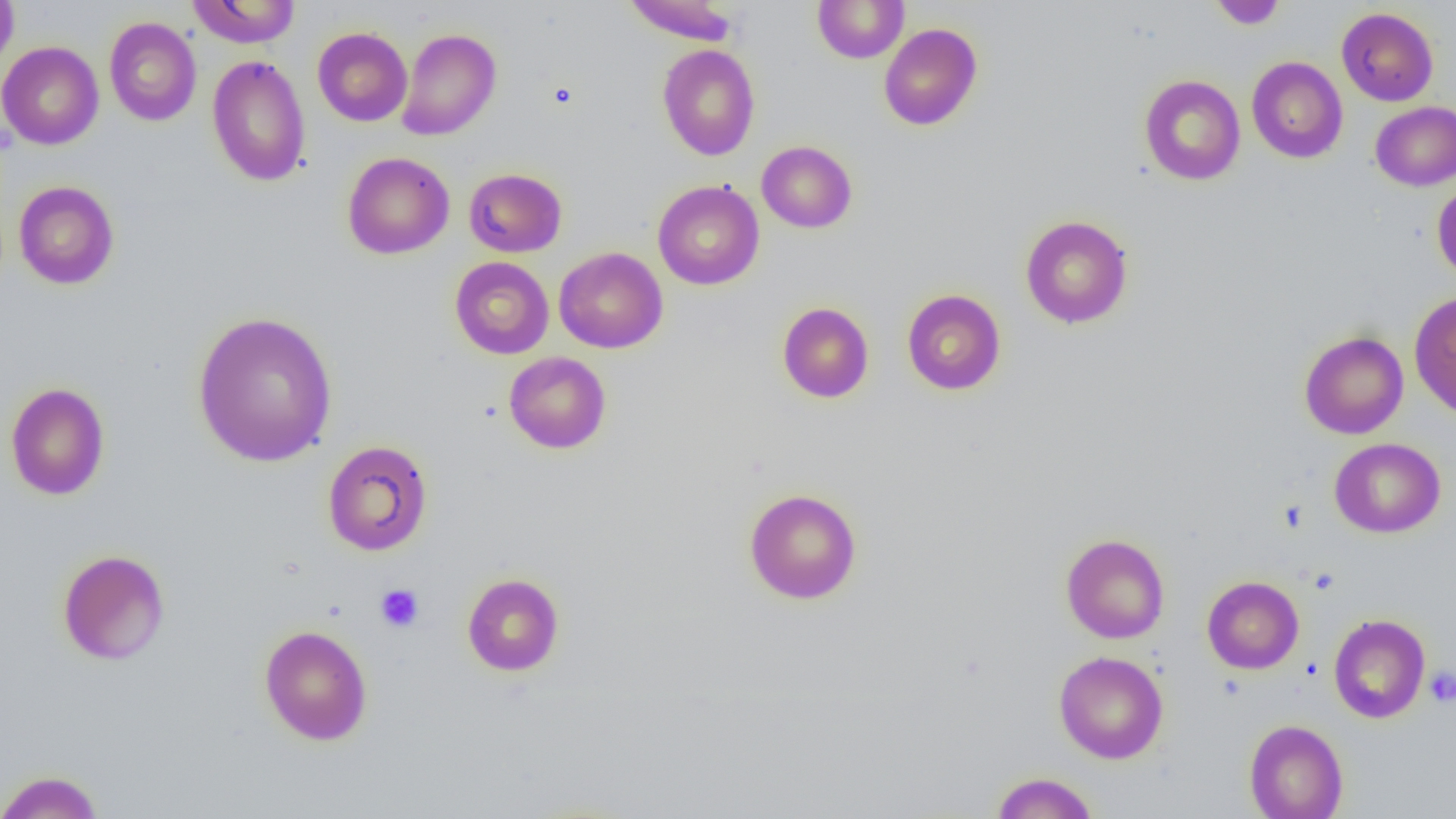
Approximate bounding boxes as [x1, y1, x2, y2] in pixels. Platelet locations: [548, 81, 578, 109], [375, 584, 424, 632], [1425, 666, 1456, 706]. Uninfected red blood cell locations: [0, 0, 19, 78], [187, 0, 300, 48], [622, 0, 739, 45], [812, 0, 909, 63], [1208, 1, 1287, 30], [1337, 7, 1438, 106], [104, 17, 202, 126], [878, 23, 982, 131], [313, 27, 412, 127], [396, 28, 501, 140], [0, 41, 104, 150], [658, 44, 760, 161], [206, 54, 311, 187], [1246, 56, 1348, 163], [1139, 74, 1246, 185], [1370, 101, 1456, 190], [756, 140, 857, 233], [342, 152, 455, 259], [464, 168, 566, 257], [652, 180, 764, 290], [1432, 180, 1456, 281], [13, 181, 119, 289], [1019, 214, 1134, 329], [554, 247, 667, 354], [449, 256, 554, 359], [902, 289, 1006, 395], [1408, 290, 1456, 418], [777, 302, 874, 403], [192, 310, 339, 467], [1299, 330, 1409, 439], [503, 351, 612, 454], [5, 382, 110, 500], [1329, 437, 1446, 538], [321, 440, 433, 556], [743, 487, 862, 604], [1060, 533, 1170, 644], [57, 549, 170, 666], [461, 572, 565, 676], [1202, 576, 1304, 674], [1328, 614, 1430, 723], [259, 624, 373, 745], [1053, 650, 1169, 764], [1244, 719, 1348, 819], [0, 769, 104, 819], [990, 772, 1099, 818]. Slide-level diagnosis: negative for blood parasites. Light microscopy. Single field of view. 1000x magnification. Image is 1456×819 pixels. Thin blood smear.